Assess the morphology of the erythrocytes.
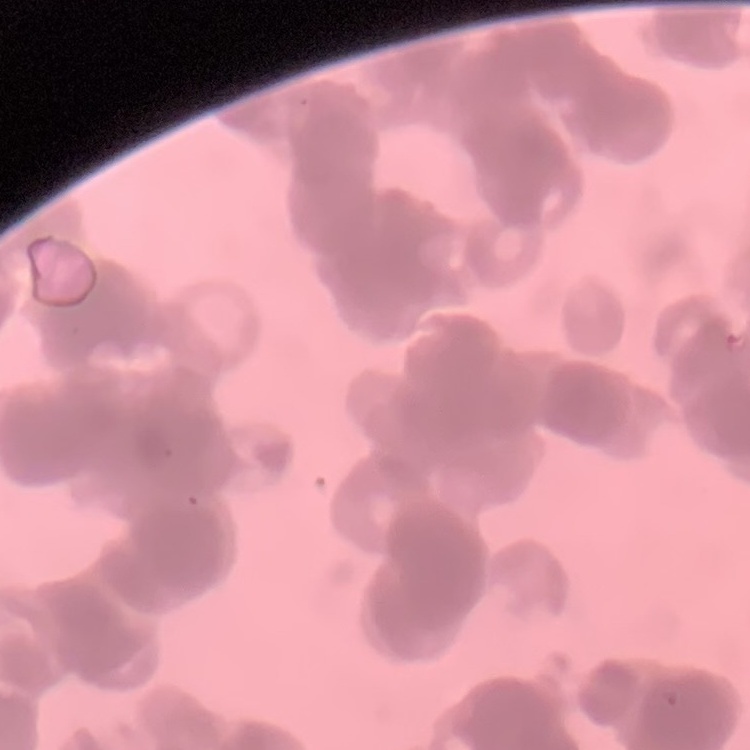
They show rouleaux formation.

Stained with either Field's or Giemsa. Square crop of a larger photomicrograph. Thin blood film.